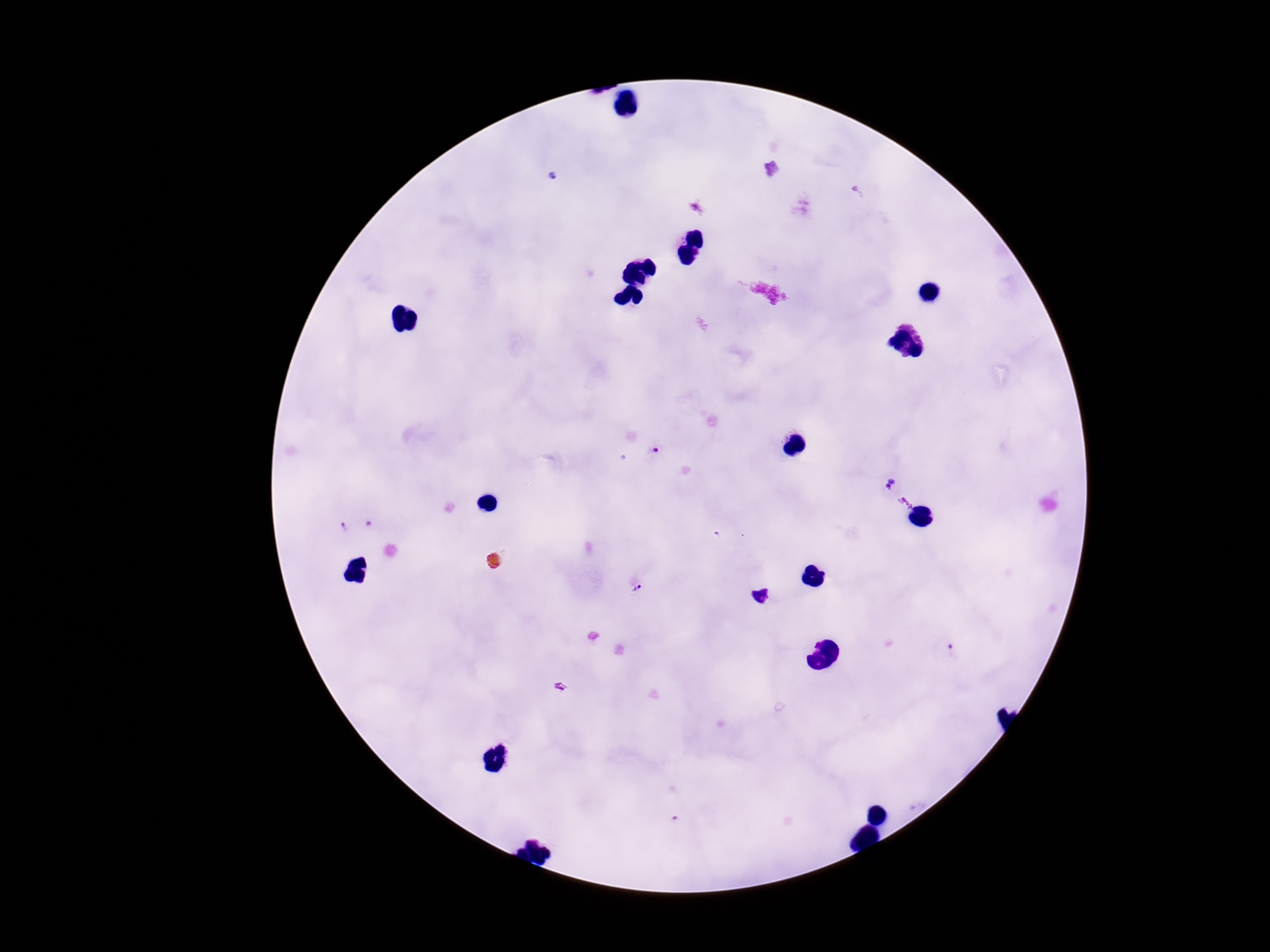
Approximate centers as [x, y] in pixels.
Summary:
  - Plasmodium parasite locations: [771, 168], [553, 177], [655, 449], [889, 484], [369, 524], [342, 525], [637, 588]
  - Stain: Giemsa
  - Preparation: thick blood film
  - Image size: 1270×952 pixels
  - Patient malaria status: positive
  - Magnification: 100x
  - Capture: smartphone camera through the microscope eyepiece
  - Field of view: one from this slide